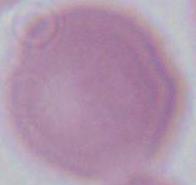

Summary:
  - Magnification: 1000x
  - Identification: erythrocyte
  - Modality: photomicrograph